State which cell type is depicted.
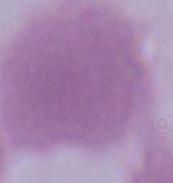

An erythrocyte.

1000x magnification. Micrograph.